Classify this cell by malaria status.
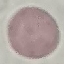

It is uninfected.

image type = automatically extracted cell patch, resized to 64 × 64 pixels
capture = smartphone camera at the microscope eyepiece
preparation = thin blood smear
stain = Giemsa